Report the malaria status of this cell.
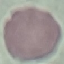

It is uninfected.

Photographed with a smartphone camera at the microscope eyepiece. Thin smear of blood. Cell patch, automatically extracted from a larger field of view and resized to 64 × 64 pixels. Giemsa-stained preparation.